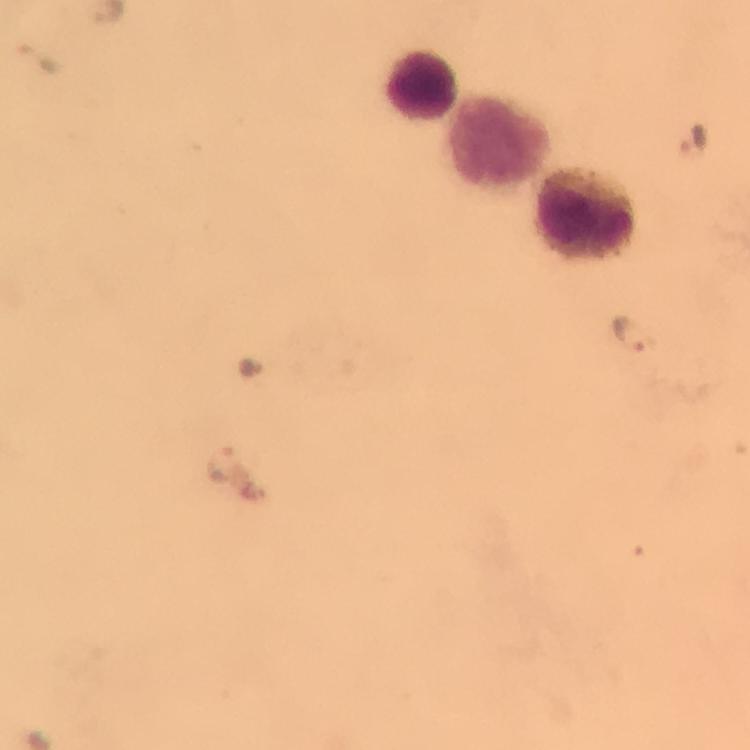

Approximate centers as [x, y] in pixels.
Summary:
  - Malaria parasite locations: [39, 56], [692, 139], [633, 332], [222, 463]
  - Leukocyte locations: [420, 83], [497, 136], [589, 213]
  - Image size: 750×750 pixels
  - Magnification: 100x
  - Immersion oil: applied
  - Capture: smartphone photograph through a microscope
  - Preparation: thick smear
  - Cropped from: one field of view
  - Context: from a malaria diagnostic workup
  - Stain: Giemsa